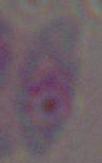

modality = photomicrograph
identification = Toxoplasma gondii
magnification = 1000x